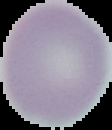
Result: no malaria parasites detected. Image is 112×130 pixels. From a thin blood film. Cell region segmented out of the field of view; the surrounding area is masked to black.